Locate every Plasmodium ovale-infected red blood cell.
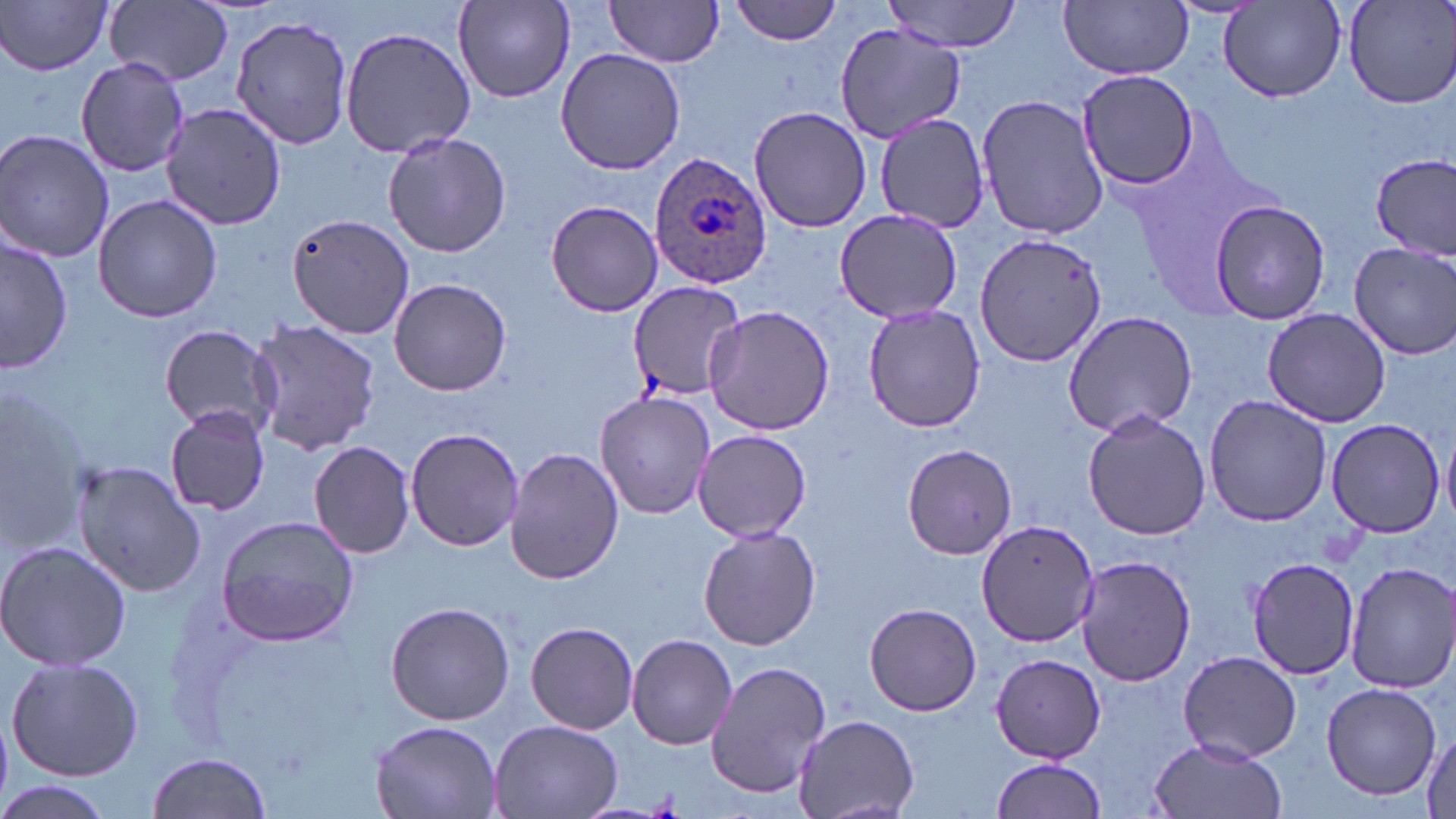
Approximate bounding boxes as [x1, y1, x2, y2] in pixels.
Plasmodium ovale-infected red blood cells: [649, 149, 774, 288].

slide-level diagnosis = Plasmodium ovale
modality = optical microscopy
image size = 1456×819 pixels
field of view = single
uninfected red blood cell locations = approximate bounding boxes as [x1, y1, x2, y2] in pixels: [453, 0, 575, 103], [729, 0, 844, 45], [1339, 0, 1456, 109], [2, 1, 115, 76], [105, 1, 233, 87], [603, 1, 726, 67], [883, 1, 1023, 53], [1059, 1, 1193, 79], [1218, 2, 1347, 101], [229, 11, 357, 151], [836, 22, 964, 144], [341, 26, 477, 158], [554, 47, 688, 174], [75, 59, 189, 176], [1077, 68, 1201, 190], [976, 94, 1108, 240], [161, 101, 288, 230], [749, 105, 873, 233], [873, 112, 991, 234], [0, 130, 115, 264], [383, 130, 512, 258], [1373, 153, 1456, 259], [92, 193, 224, 322], [1205, 198, 1332, 322], [544, 199, 665, 317], [833, 209, 963, 323], [288, 212, 415, 340], [973, 232, 1106, 368], [2, 234, 74, 374], [1350, 243, 1456, 358], [389, 279, 512, 395], [627, 281, 745, 400], [862, 303, 985, 433], [704, 305, 836, 436], [1262, 308, 1392, 427], [1062, 311, 1197, 436], [247, 318, 380, 458], [157, 324, 282, 437], [594, 390, 716, 520], [1204, 393, 1331, 527], [165, 404, 274, 515], [1081, 408, 1211, 541], [1324, 418, 1446, 536], [405, 427, 522, 552], [692, 429, 811, 541], [309, 441, 416, 559], [901, 443, 1019, 558], [505, 448, 624, 585], [72, 459, 204, 596], [215, 515, 361, 648], [978, 519, 1098, 646], [698, 525, 821, 650], [0, 538, 132, 673], [1245, 555, 1360, 682], [1076, 556, 1198, 686], [1347, 562, 1456, 693], [384, 602, 515, 725], [863, 603, 982, 716], [526, 621, 639, 734], [628, 633, 737, 749], [1176, 651, 1303, 763], [990, 652, 1106, 762], [5, 657, 145, 782], [706, 661, 831, 800], [1322, 680, 1443, 800], [792, 713, 919, 816], [487, 718, 624, 819], [370, 720, 501, 818], [1420, 726, 1456, 817], [1149, 736, 1285, 819], [145, 751, 273, 819], [990, 756, 1107, 819], [0, 780, 118, 819]
stain = May-Grünwald-Giemsa
preparation = thin blood smear
magnification = 1000x